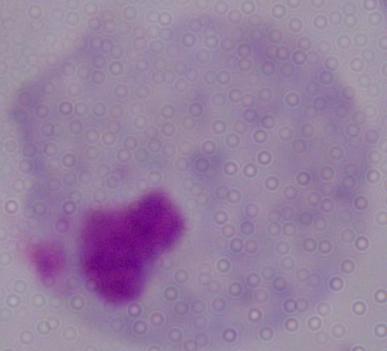 Micrograph. Captured at 1000x magnification. A trichomonad is shown.